Classify this cell by malaria status.
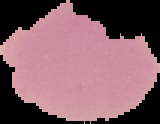

Uninfected.

Segmented cell region on a black background. From a thin blood smear. Image is 160×124 pixels.